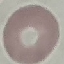
Summary:
  - Result: negative for malaria parasites
  - Preparation: thin blood film
  - Stain: Giemsa
  - Capture: smartphone camera at the microscope eyepiece
  - Image type: cell patch, automatically extracted from a larger field of view and resized to 64 × 64 pixels